State the blood parasite species.
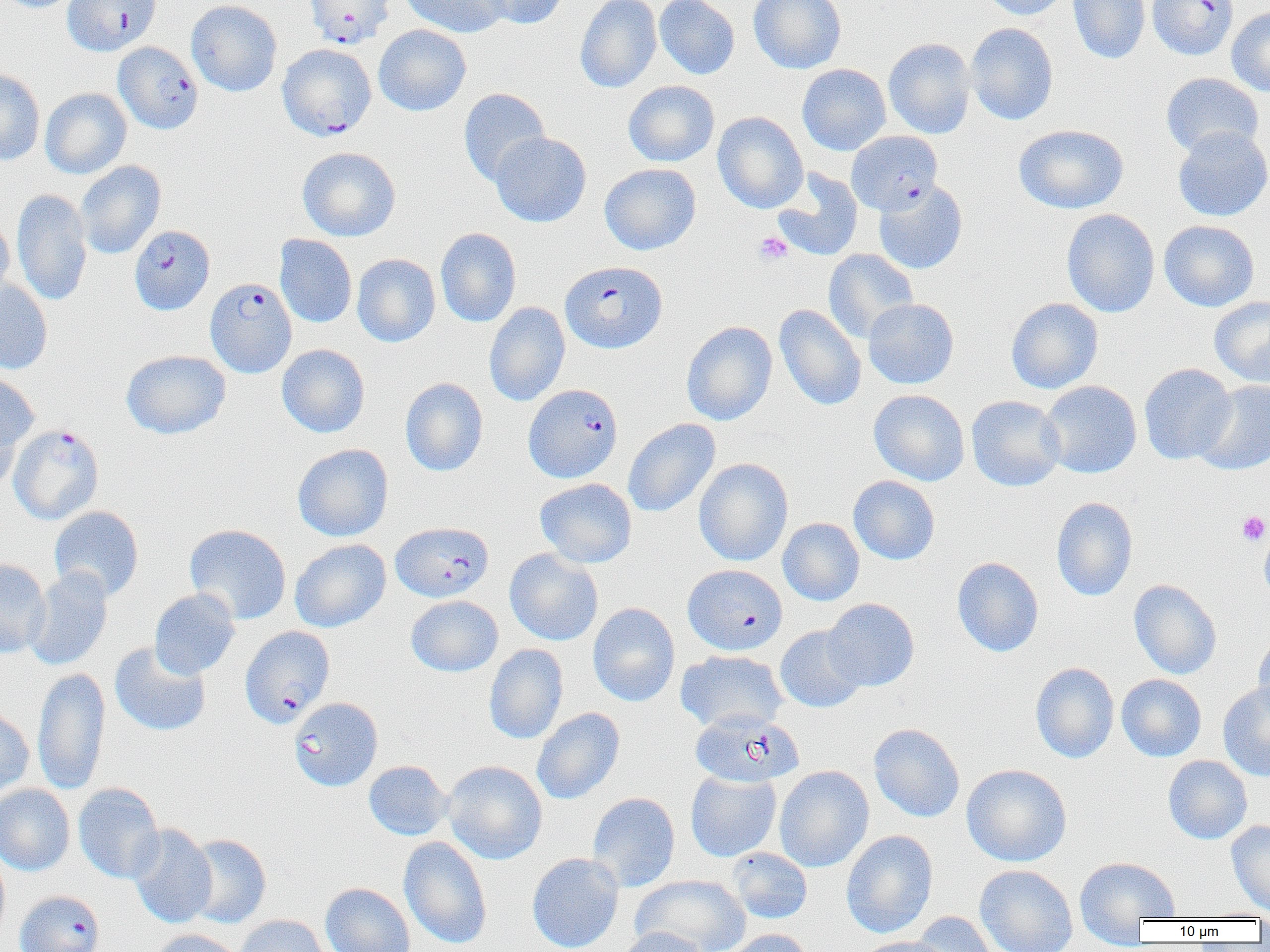

Plasmodium falciparum.

Summary:
  - Coordinate format: approximate bounding boxes as (x1, y1, x2, y2) in pixels
  - Uninfected red blood cell locations (subset): (0, 0, 84, 12), (186, 0, 282, 96), (400, 0, 511, 37), (477, 0, 569, 29), (575, 0, 662, 93), (654, 0, 740, 79), (749, 0, 847, 74), (981, 0, 1072, 20), (1068, 0, 1150, 64), (1227, 7, 1270, 96), (965, 23, 1058, 125), (373, 24, 471, 116), (883, 37, 976, 139), (797, 63, 891, 155), (0, 67, 45, 165), (1160, 72, 1264, 158), (623, 80, 720, 167), (40, 88, 132, 179), (458, 88, 550, 186), (713, 111, 808, 213), (1014, 124, 1129, 214), (1173, 126, 1270, 221), (489, 132, 591, 227), (297, 146, 400, 242), (75, 161, 166, 259), (599, 163, 701, 255), (772, 168, 863, 261), (874, 181, 968, 274), (12, 189, 92, 306), (1061, 208, 1160, 317), (0, 217, 14, 304), (1159, 220, 1259, 311), (435, 227, 521, 327), (274, 234, 357, 328), (823, 249, 919, 342), (352, 254, 440, 347), (0, 279, 53, 374), (1209, 296, 1270, 387), (1006, 297, 1103, 394), (863, 298, 959, 389), (484, 301, 570, 407), (774, 304, 866, 411), (681, 321, 777, 425), (277, 344, 370, 437), (121, 350, 231, 439), (1139, 363, 1237, 464), (0, 372, 39, 467), (400, 378, 488, 476), (1039, 380, 1142, 478), (1194, 380, 1270, 475), (869, 390, 969, 486), (966, 395, 1066, 491), (0, 406, 23, 495), (623, 418, 720, 518), (292, 444, 393, 541), (694, 458, 793, 566), (848, 475, 940, 565), (535, 478, 637, 568), (1052, 497, 1138, 601), (49, 506, 144, 601), (778, 517, 864, 605), (1259, 522, 1270, 605), (184, 523, 292, 624), (290, 539, 391, 632), (504, 549, 603, 646), (952, 556, 1044, 657), (0, 559, 51, 657), (24, 568, 113, 671), (1129, 579, 1222, 679), (149, 588, 240, 679), (406, 596, 503, 677), (823, 598, 920, 691), (588, 602, 680, 706), (775, 625, 867, 712), (1253, 631, 1270, 718), (109, 641, 211, 737), (484, 644, 568, 744), (675, 650, 788, 733), (1030, 662, 1120, 763), (32, 667, 110, 796), (1116, 674, 1206, 761), (1218, 680, 1270, 781), (289, 697, 383, 791), (0, 706, 34, 798), (532, 707, 625, 805), (869, 723, 965, 822), (1163, 755, 1252, 844), (363, 760, 453, 841), (443, 760, 547, 864), (961, 763, 1072, 867), (774, 765, 874, 872), (685, 770, 781, 861), (73, 783, 164, 884), (0, 784, 74, 875), (588, 792, 680, 892), (1226, 820, 1270, 915), (128, 824, 217, 929), (841, 830, 937, 938), (184, 834, 271, 928), (399, 836, 492, 949), (728, 847, 812, 924), (0, 853, 10, 947), (527, 853, 623, 952), (1074, 856, 1181, 940), (975, 864, 1078, 952), (631, 874, 750, 952), (320, 882, 415, 952), (910, 912, 999, 952), (233, 914, 331, 952), (617, 927, 710, 952), (150, 929, 245, 952), (721, 929, 812, 952), (854, 936, 952, 952)
  - Platelet locations: (753, 232, 793, 265), (1237, 511, 1269, 545)
  - Plasmodium falciparum-infected red blood cell locations (subset): (62, 0, 161, 56), (303, 0, 394, 48), (1147, 0, 1237, 59), (277, 43, 377, 140), (848, 133, 944, 218), (129, 225, 215, 314), (560, 261, 667, 353), (205, 278, 296, 377), (523, 383, 622, 482), (9, 423, 104, 525), (391, 522, 494, 602), (682, 564, 787, 655), (240, 625, 335, 727), (690, 709, 803, 788), (14, 890, 104, 952)
  - Image size: 1270×952 pixels
  - Field of view: single
  - Preparation: thin blood smear
  - Magnification: 1000x
  - Modality: light microscopy